Give the position of every malaria parasite.
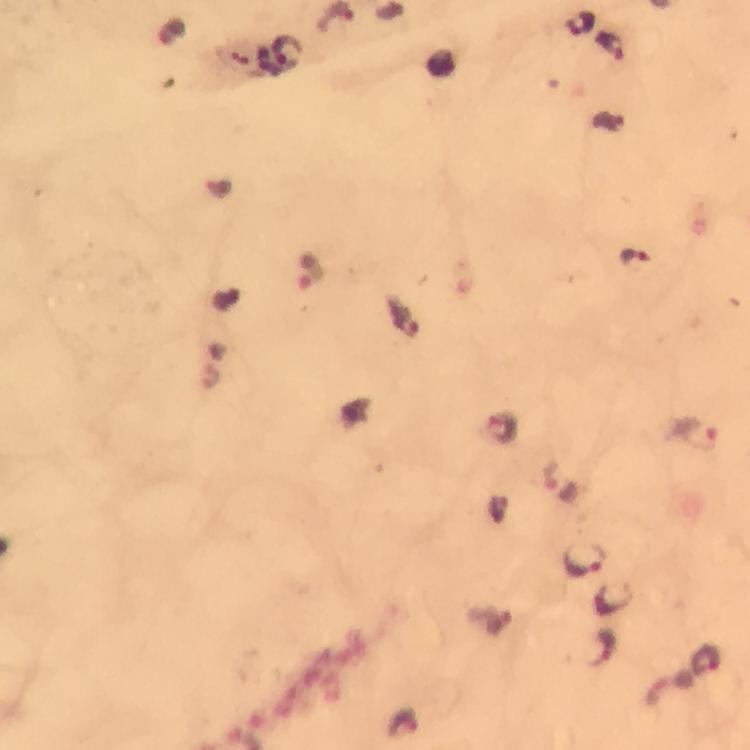
Approximate centers as (x, y) in pixels.
Malaria parasites: (579, 22), (611, 46), (636, 255), (310, 269), (403, 317), (502, 425), (697, 433), (585, 558).

Image is 750×750 pixels. Photographed through the microscope with a smartphone camera. Giemsa stain. From a malaria diagnostic workup. Cropped region of a single field of view. Immersion oil applied. Thick blood smear. 100x magnification.